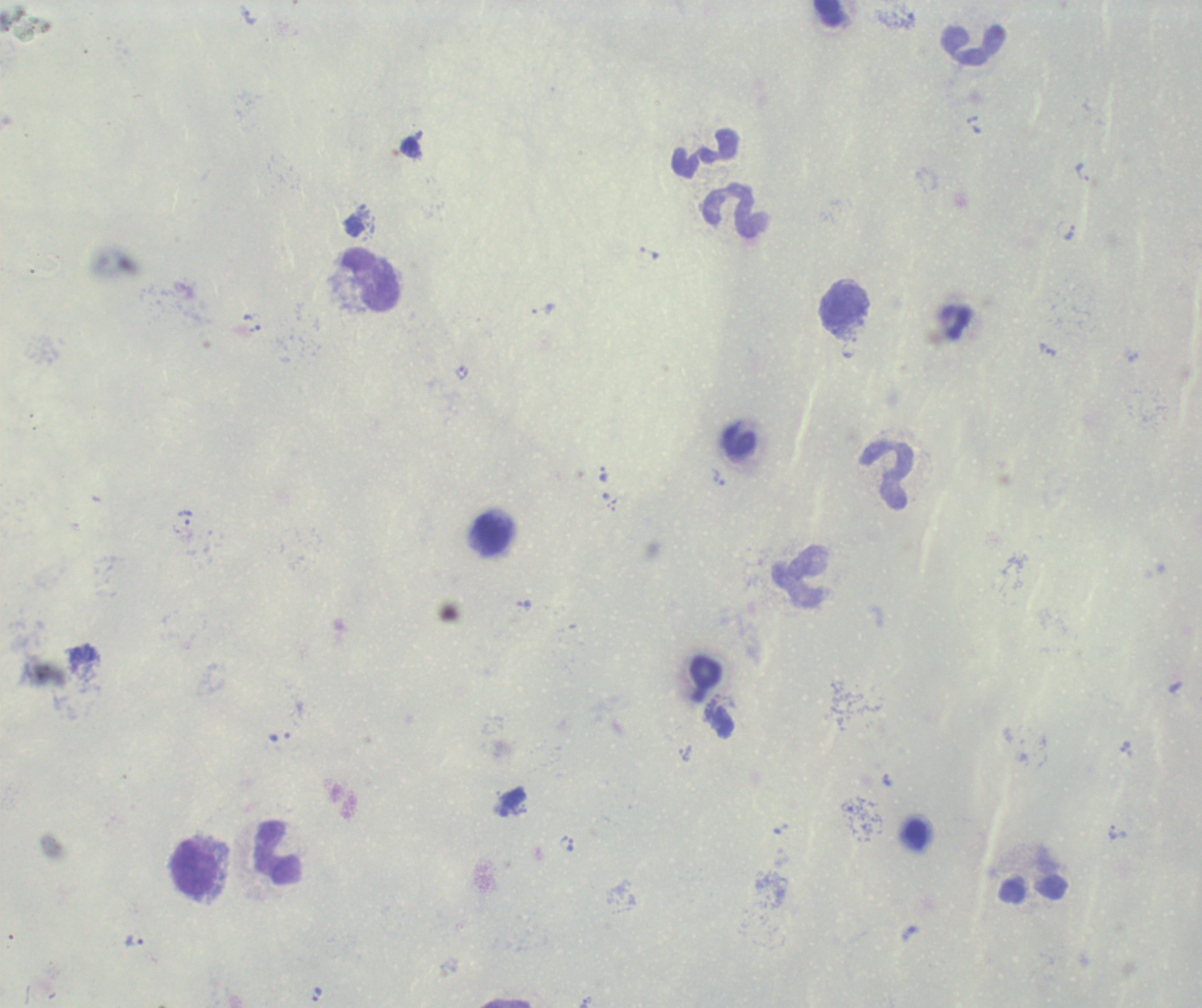
Approximate object centers, in pixels from the top-left corner.
Summary:
  - Trophozoite locations: (x=1082, y=172), (x=1069, y=232), (x=650, y=253), (x=543, y=309), (x=255, y=329), (x=1048, y=350), (x=603, y=474), (x=718, y=477), (x=184, y=517), (x=280, y=736), (x=684, y=753), (x=886, y=780), (x=1113, y=832), (x=566, y=843), (x=134, y=941), (x=317, y=993), (x=585, y=1000)
  - Leukocyte locations: (x=972, y=45), (x=705, y=153), (x=735, y=212), (x=369, y=280), (x=844, y=305), (x=740, y=445), (x=886, y=475), (x=491, y=533), (x=801, y=578), (x=705, y=673), (x=916, y=833), (x=278, y=853), (x=194, y=867)
  - Background quality: unsatisfactory
  - Context: previously used in a real diagnosis
  - Preparation: thick blood smear
  - Field of view: one from this slide
  - Image size: 1202×1008 pixels
  - Stain: Romanowsky
  - Magnification: 100x
  - Result: Plasmodium parasites detected